Outline each blood parasite and name the species.
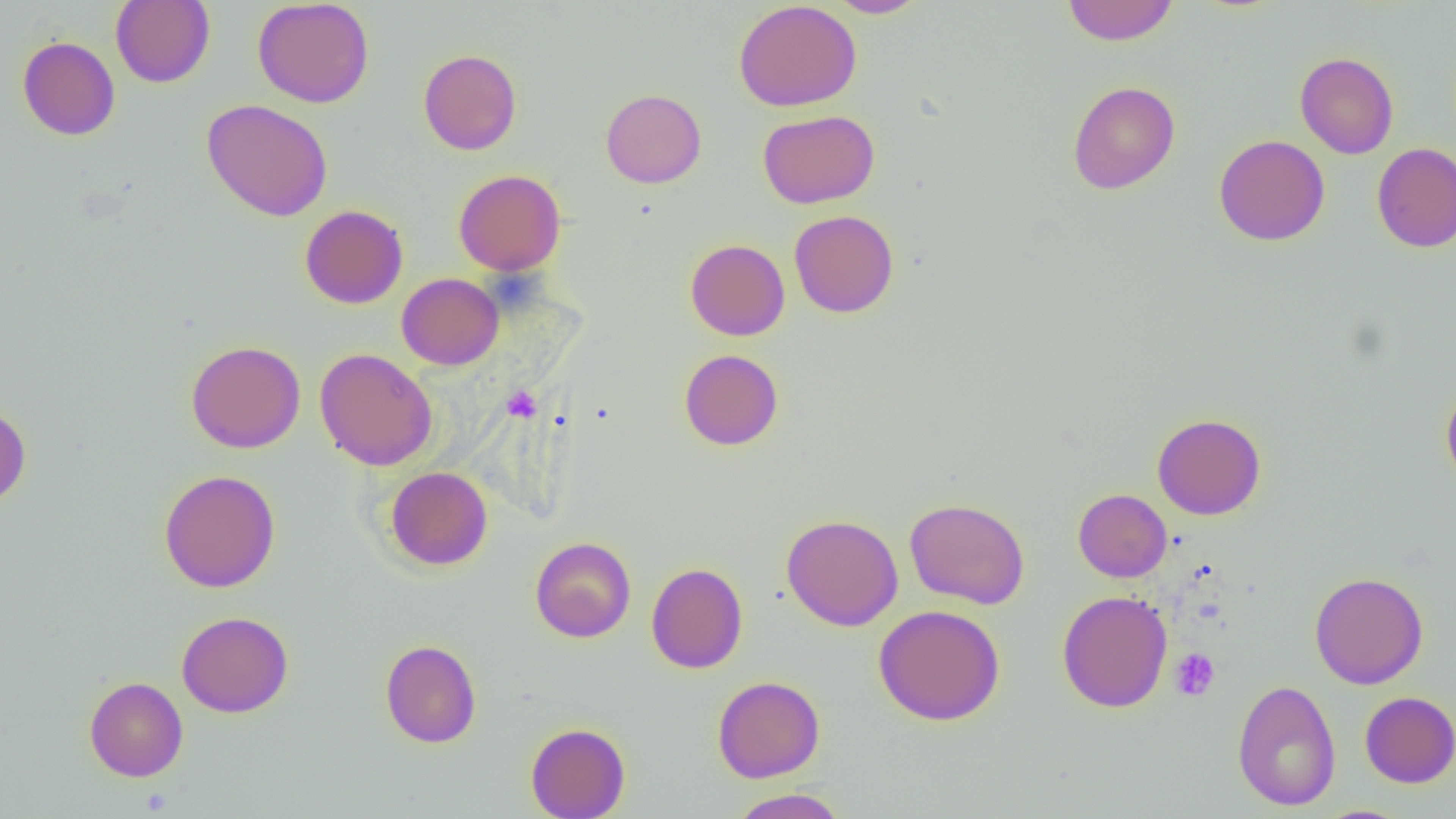
No blood parasites observed.

{
  "slide_level_diagnosis": "negative for blood parasites",
  "image_size": "1456×819 pixels",
  "magnification": "1000x",
  "field_of_view": "one of a larger specimen",
  "platelet_locations": "approximate bounding boxes as [x1, y1, x2, y2] in pixels: [501, 386, 542, 423], [1169, 648, 1219, 701]",
  "modality": "optical microscopy",
  "uninfected_red_blood_cell_locations": "approximate bounding boxes as [x1, y1, x2, y2] in pixels: [111, 0, 215, 88], [252, 0, 375, 108], [825, 0, 931, 18], [1062, 0, 1178, 46], [733, 1, 862, 112], [17, 36, 120, 140], [418, 49, 522, 155], [1295, 52, 1398, 159], [1067, 80, 1180, 195], [601, 89, 706, 188], [202, 99, 333, 221], [758, 109, 879, 209], [1214, 134, 1330, 246], [1371, 142, 1456, 253], [453, 169, 565, 275], [299, 204, 408, 309], [789, 210, 899, 318], [685, 239, 790, 340], [396, 273, 503, 370], [186, 340, 305, 453], [314, 348, 437, 471], [679, 349, 784, 450], [1441, 384, 1456, 491], [0, 404, 31, 507], [1152, 413, 1266, 520], [385, 466, 493, 570], [159, 469, 280, 593], [1073, 488, 1172, 582], [904, 498, 1030, 609], [780, 514, 903, 631], [530, 537, 636, 643], [646, 562, 748, 674], [1309, 572, 1428, 689], [1057, 590, 1172, 713], [874, 605, 1005, 725], [177, 611, 293, 718], [380, 639, 481, 748], [84, 676, 188, 781], [712, 676, 825, 782], [1231, 678, 1340, 811], [1359, 691, 1456, 788], [525, 722, 630, 818], [728, 788, 849, 818]",
  "preparation": "thin blood smear"
}